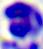
Summary:
  - Magnification: 400x
  - Modality: photomicrograph
  - Identification: leukocyte